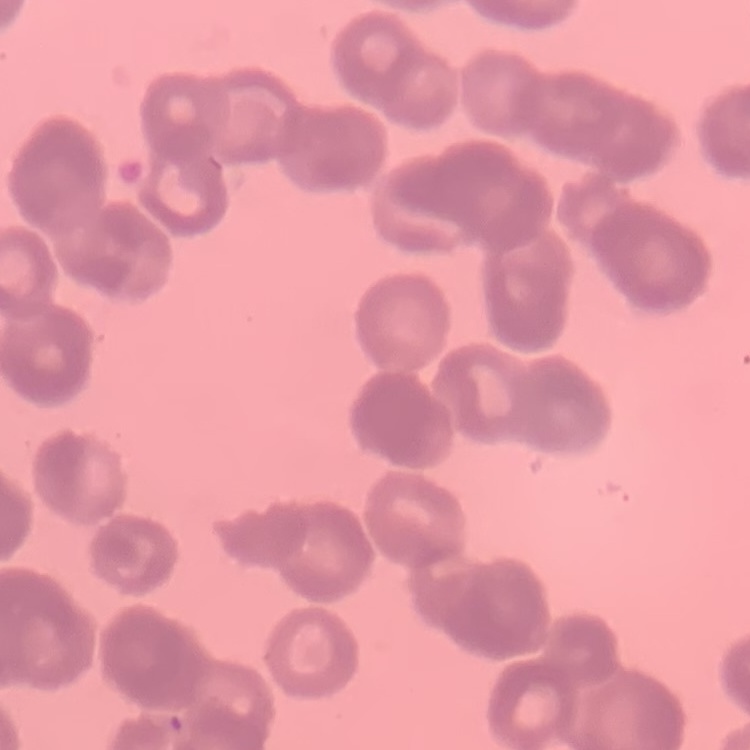
The erythrocytes show rouleaux formation. Thin blood film. One tile cut from a larger photomicrograph. Field's or Giemsa stain.